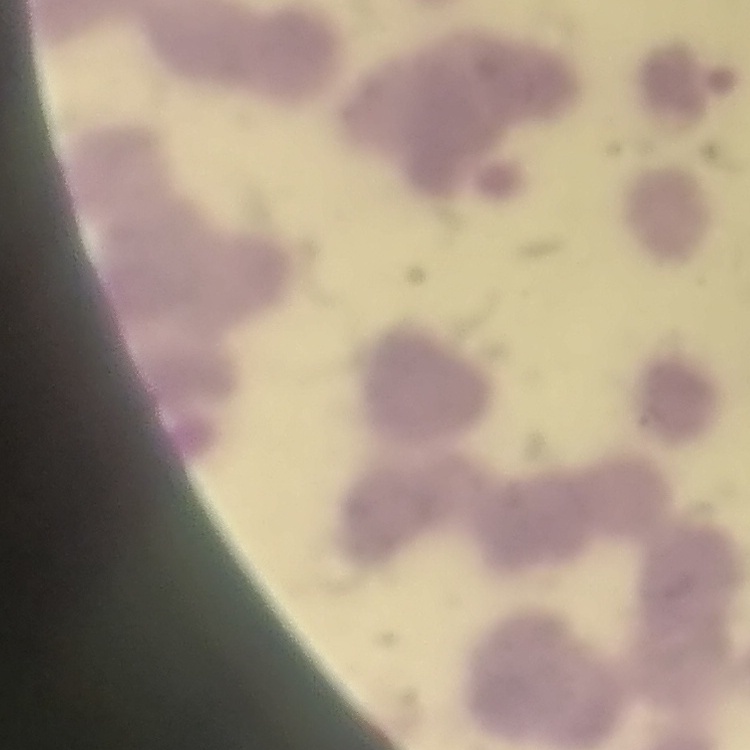 The red blood cells show rouleaux formation. One tile cut from a larger photomicrograph. Thin blood film. Stained with either Field's or Giemsa.